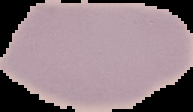 Image is 193×112 pixels. Malaria status: uninfected. From a thin blood film. The area outside the segmented cell region is set to black.